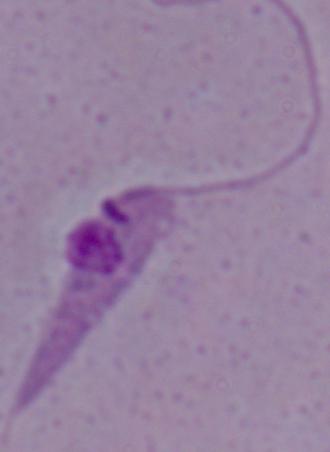

identification = Leishmania
modality = micrograph
magnification = 1000x